Locate and identify every blood parasite.
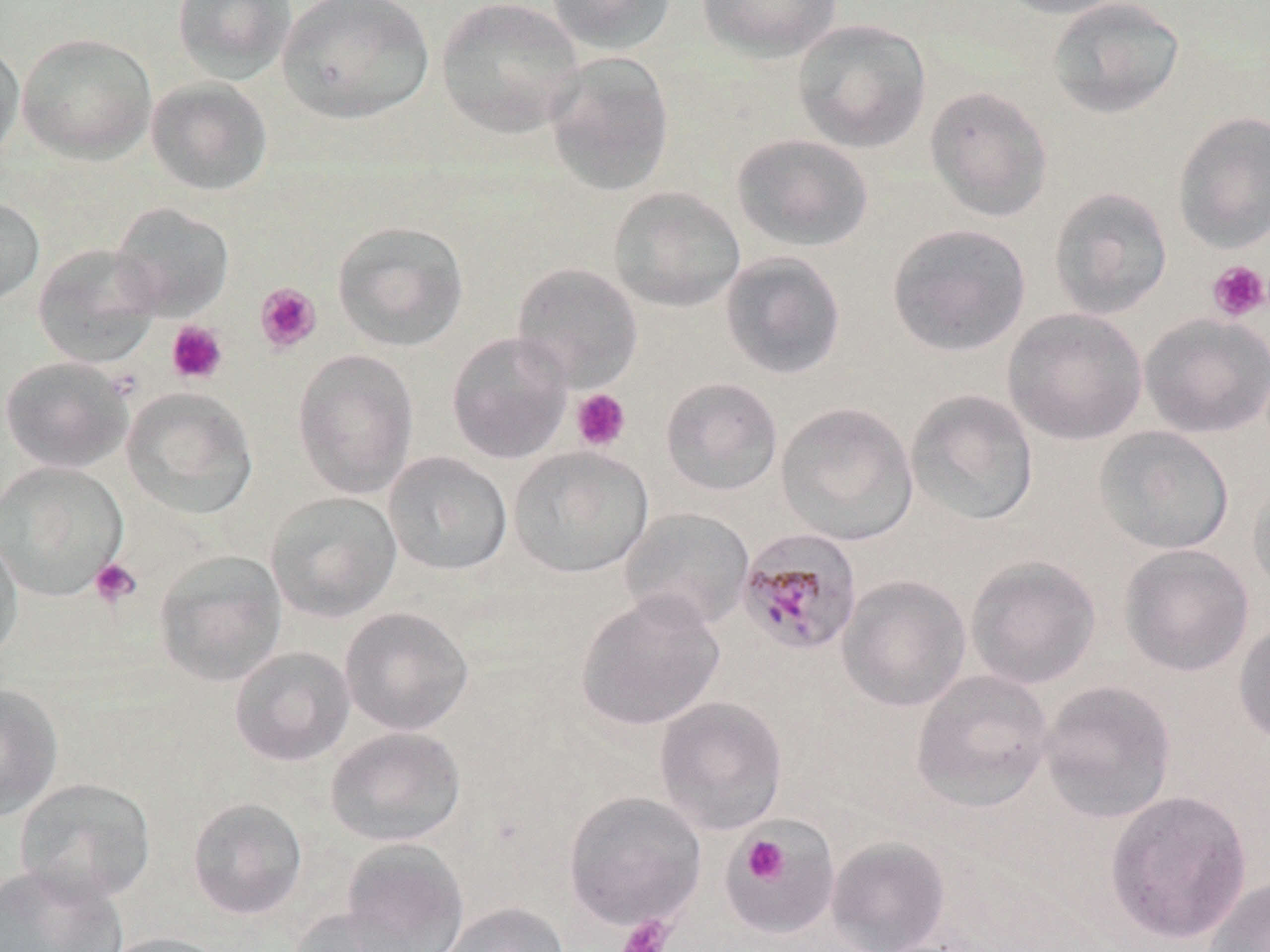
Approximate bounding boxes as (x1,y1)-(x2,y2) corner pairs in pixels.
Plasmodium malariae-infected red blood cells: (736,527)-(863,656).
No Plasmodium falciparum, Plasmodium ovale, Plasmodium vivax, Babesia divergens, or Trypanosoma brucei observed.

Summary:
  - Platelet locations: (1207,260)-(1269,321), (254,282)-(321,354), (166,320)-(228,385), (571,388)-(631,452), (89,557)-(142,608), (742,836)-(788,883), (616,915)-(675,952)
  - Uninfected red blood cell locations: (172,0)-(298,85), (276,0)-(434,124), (436,0)-(585,138), (545,0)-(677,55), (695,0)-(843,62), (993,0)-(1135,20), (1046,0)-(1186,119), (792,19)-(931,154), (17,32)-(157,163), (0,40)-(25,165), (542,52)-(676,197), (146,77)-(272,196), (925,85)-(1053,222), (1172,111)-(1270,253), (731,133)-(874,252), (608,186)-(746,313), (1048,186)-(1173,319), (0,196)-(45,308), (111,201)-(234,321), (332,220)-(470,352), (886,222)-(1032,357), (32,243)-(163,368), (719,251)-(847,380), (511,262)-(644,392), (1003,307)-(1147,446), (1140,313)-(1270,438), (447,331)-(573,464), (292,349)-(419,499), (1,355)-(134,473), (660,376)-(783,497), (121,387)-(258,519), (905,388)-(1039,527), (776,401)-(919,546), (1094,425)-(1234,555), (507,446)-(653,578), (383,451)-(512,576), (0,460)-(129,601), (1247,470)-(1270,599), (265,491)-(402,623), (618,507)-(755,631), (0,530)-(23,666), (1119,543)-(1254,677), (153,549)-(287,687), (965,554)-(1101,690), (836,574)-(971,712), (575,589)-(725,732), (340,606)-(474,735), (1233,616)-(1270,745), (229,646)-(355,766), (910,669)-(1054,812), (1038,679)-(1177,823), (0,682)-(63,821), (653,696)-(788,835), (325,726)-(466,847), (14,777)-(157,905), (1104,789)-(1253,945), (563,791)-(706,931), (186,797)-(308,920), (720,818)-(841,938), (825,836)-(951,951), (341,838)-(470,952), (0,863)-(128,951), (1202,875)-(1270,952), (438,901)-(570,952), (286,907)-(422,952), (99,931)-(233,952)
  - Slide-level diagnosis: Plasmodium malariae
  - Image size: 1270×952 pixels
  - Stain: May-Grünwald-Giemsa
  - Preparation: thin blood smear
  - Field of view: one of a larger specimen
  - Modality: light microscopy
  - Magnification: 1000x